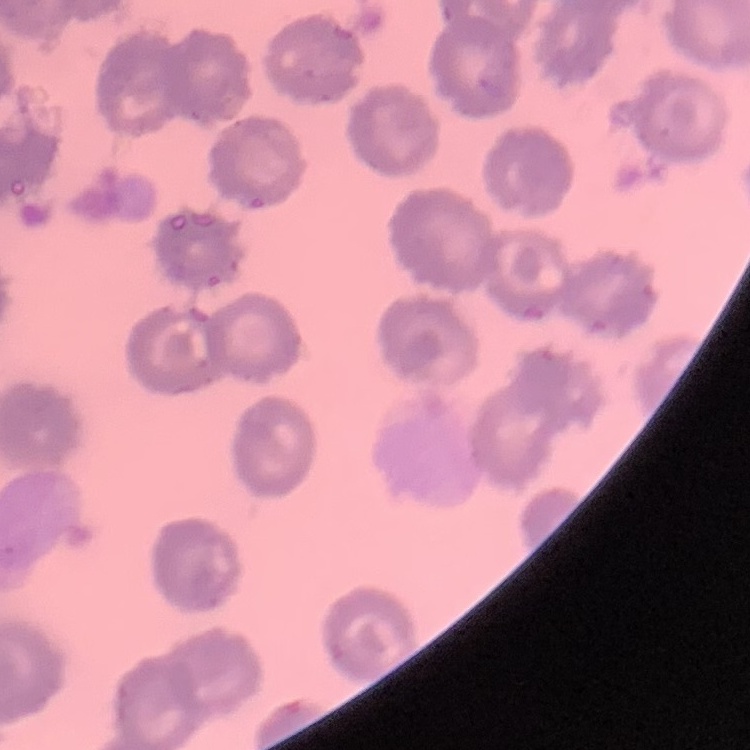
red blood cell morphology = no rouleaux formation
image type = square crop of a larger photomicrograph
stain = Field's or Giemsa
preparation = thin blood film